Name the blood parasite species.
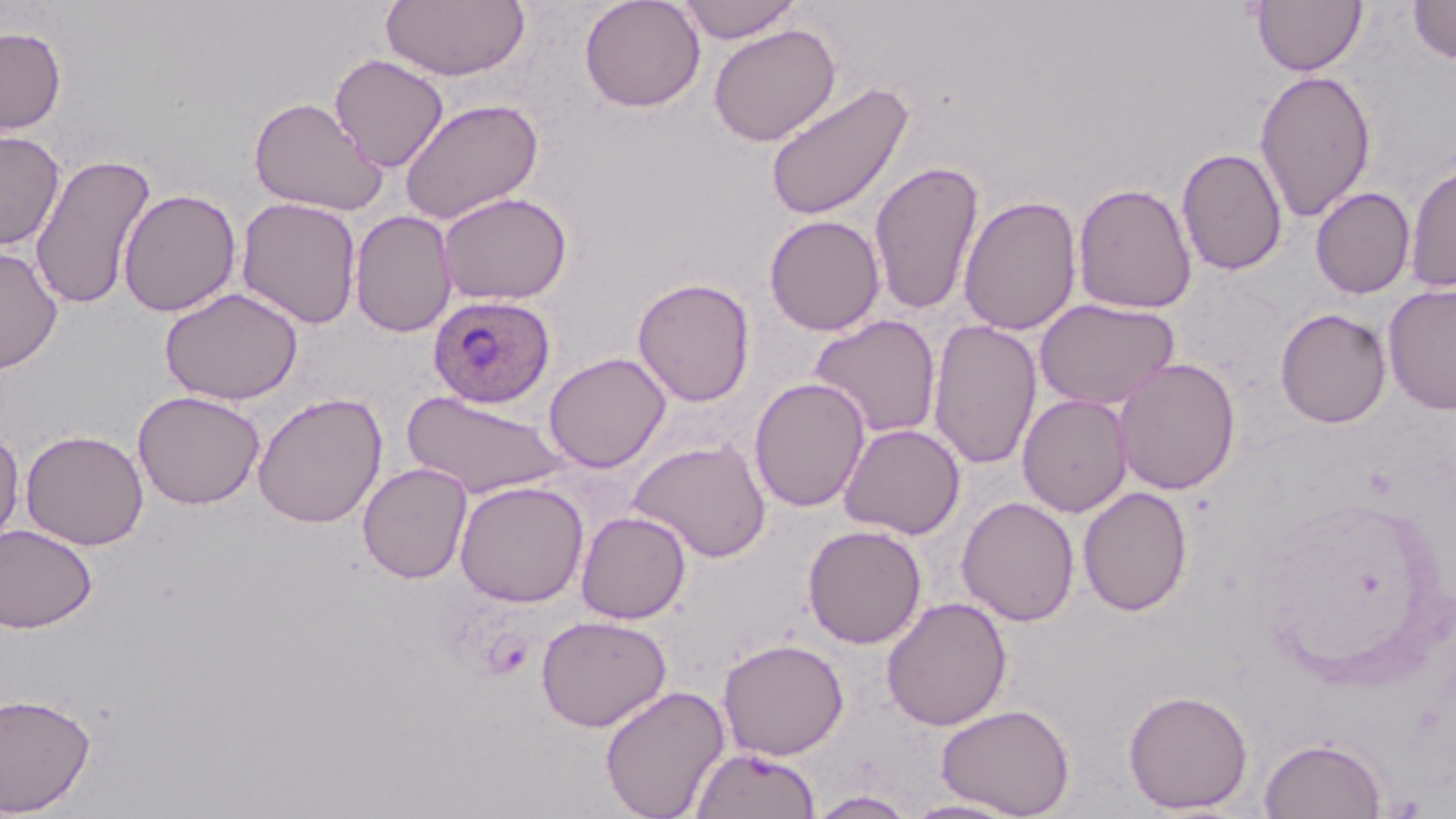

Plasmodium ovale.

Summary:
  - Coordinate format: approximate bounding boxes as (x1,y1)-(x2,y2) corner pairs in pixels
  - Uninfected red blood cell locations: (381,0)-(531,81), (578,0)-(706,113), (677,0)-(801,44), (1252,0)-(1367,76), (1407,0)-(1456,64), (708,23)-(841,146), (0,26)-(67,134), (329,54)-(449,172), (1253,69)-(1378,224), (765,80)-(915,223), (248,95)-(388,216), (399,98)-(543,225), (0,128)-(65,250), (1177,147)-(1288,276), (30,153)-(156,311), (869,158)-(984,316), (1404,160)-(1456,294), (1072,182)-(1197,314), (1311,187)-(1416,298), (118,188)-(241,317), (436,191)-(573,306), (958,195)-(1081,337), (236,197)-(362,330), (349,210)-(458,338), (764,215)-(885,336), (0,245)-(63,374), (632,277)-(756,407), (1383,282)-(1456,415), (159,286)-(304,405), (1035,298)-(1180,411), (1275,308)-(1392,428), (808,314)-(942,440), (928,320)-(1041,471), (543,352)-(672,473), (1114,357)-(1241,495), (749,377)-(870,513), (402,389)-(570,499), (132,390)-(266,510), (252,392)-(387,529), (1017,394)-(1133,518), (839,423)-(965,540), (0,426)-(24,551), (20,429)-(149,550), (629,438)-(772,563), (357,462)-(472,584), (454,480)-(589,607), (1077,486)-(1193,617), (957,496)-(1080,627), (575,510)-(692,624), (0,523)-(98,634), (802,524)-(927,649), (880,596)-(1012,731), (535,614)-(672,732), (718,637)-(849,760), (600,684)-(730,819), (1123,688)-(1254,814), (0,691)-(97,816), (937,703)-(1075,818), (1259,737)-(1387,818), (689,746)-(820,818), (808,790)-(918,818), (900,798)-(1027,818)
  - Plasmodium ovale-infected red blood cell locations: (427,294)-(556,409)
  - Modality: light microscopy
  - Magnification: 1000x
  - Preparation: thin blood smear
  - Field of view: single
  - Image size: 1456×819 pixels
  - Stain: May-Grünwald-Giemsa